Assess the morphology of the red blood cells.
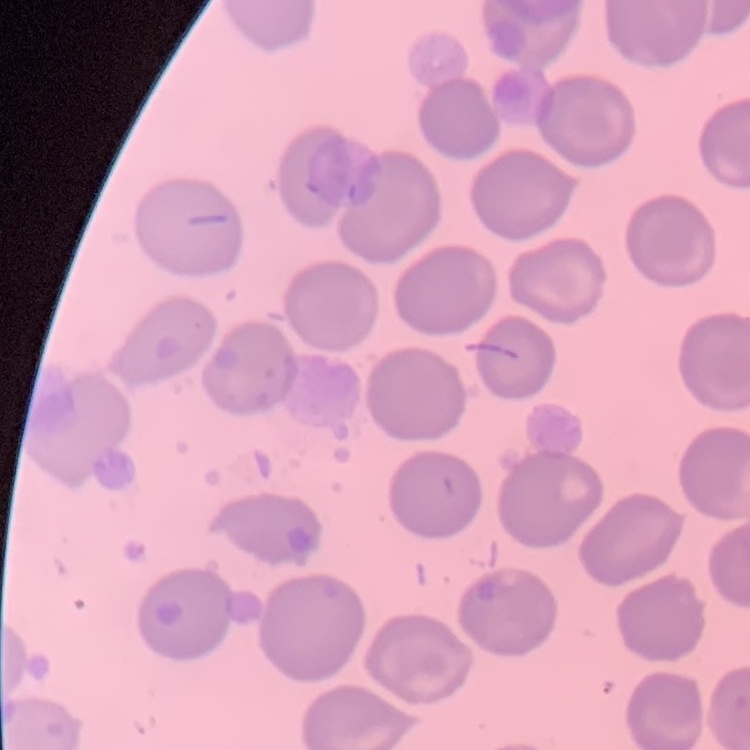
They show no rouleaux formation.

Summary:
  - Image type: square crop of a larger photomicrograph
  - Stain: Field's or Giemsa
  - Preparation: thin peripheral smear